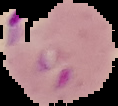

Result: Plasmodium parasites detected. Image is 118×106 pixels. The area outside the segmented cell region is set to black. From a thin blood smear.